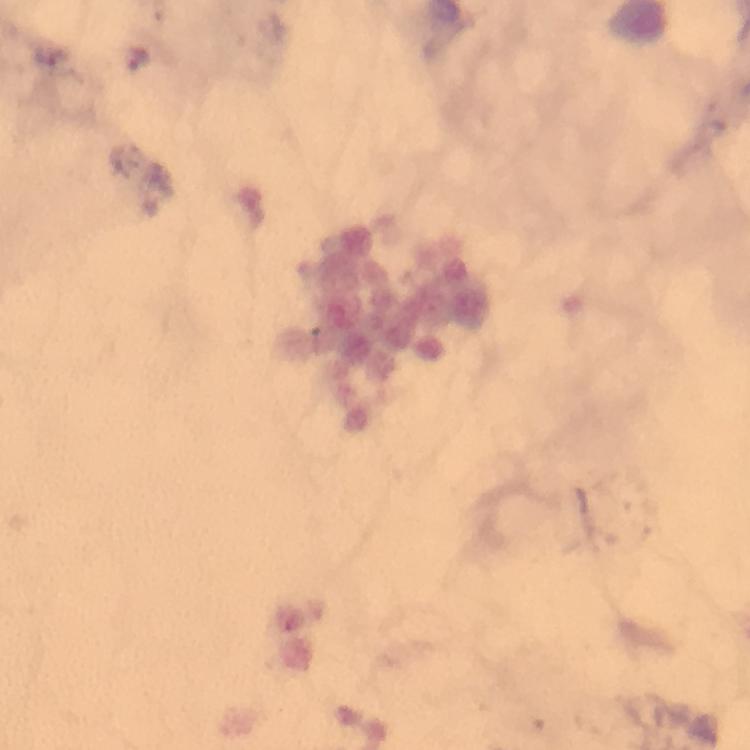

Approximate centers as [x, y] in pixels.
Summary:
  - Plasmodium parasite locations: [138, 58]
  - Immersion oil: used
  - Image size: 750×750 pixels
  - Capture: smartphone mounted on the microscope
  - Context: from a malaria diagnostic workup
  - Stain: Giemsa
  - Magnification: 100x
  - Cropped from: one field of view
  - Preparation: thick blood smear